Locate every Babesia divergens-infected red blood cell.
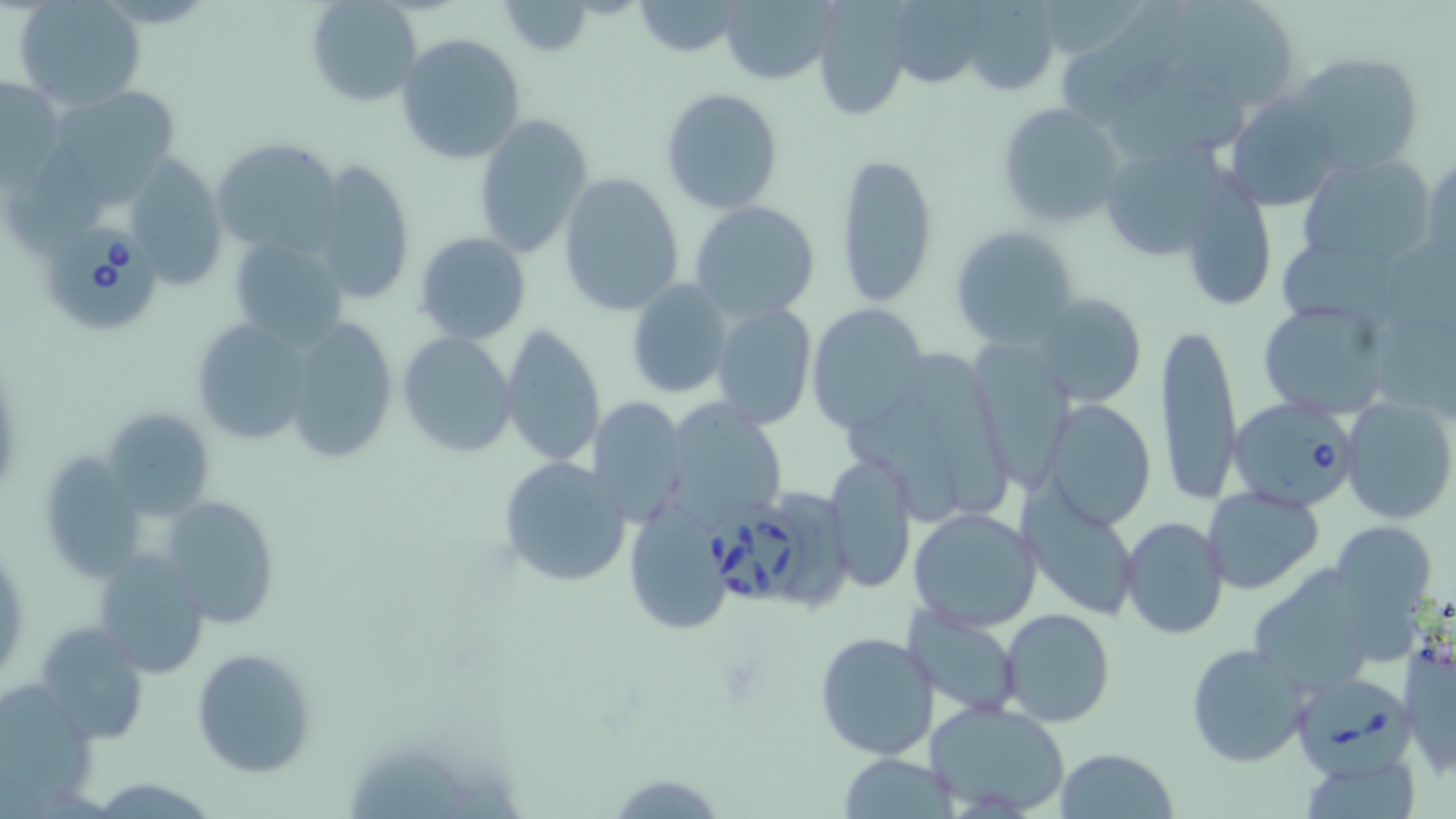

Approximate bounding boxes as (x1, y1, x2, y2) in pixels.
Babesia divergens-infected red blood cells: (45, 223, 158, 331), (1232, 397, 1360, 514), (706, 503, 811, 608), (1288, 673, 1414, 776).

Summary:
  - Uninfected red blood cell locations: (305, 0, 422, 107), (964, 0, 1058, 92), (1182, 0, 1300, 102), (13, 1, 147, 112), (499, 1, 595, 57), (633, 1, 744, 56), (720, 1, 838, 85), (1064, 4, 1190, 121), (813, 5, 908, 120), (395, 33, 525, 165), (1110, 50, 1250, 162), (1293, 51, 1424, 175), (1, 74, 68, 186), (49, 82, 183, 195), (660, 88, 782, 213), (1224, 92, 1341, 209), (994, 101, 1127, 228), (474, 112, 594, 259), (212, 138, 343, 262), (1110, 145, 1233, 261), (837, 152, 938, 307), (1422, 153, 1455, 272), (1296, 154, 1434, 267), (16, 155, 109, 248), (133, 155, 229, 290), (303, 158, 417, 308), (558, 171, 687, 317), (1179, 174, 1276, 312), (688, 201, 821, 323), (950, 226, 1081, 349), (414, 232, 531, 344), (223, 233, 347, 348), (1283, 243, 1402, 325), (626, 278, 732, 398), (1028, 291, 1148, 408), (1255, 295, 1395, 417), (711, 301, 816, 430), (806, 304, 928, 434), (188, 314, 318, 447), (282, 317, 400, 464), (1156, 318, 1241, 507), (500, 324, 605, 470), (397, 332, 519, 458), (971, 342, 1080, 491), (916, 359, 1012, 515), (843, 387, 976, 523), (1042, 397, 1156, 529), (585, 398, 689, 524), (1341, 398, 1456, 525), (663, 400, 789, 528), (101, 408, 215, 520), (38, 450, 150, 584), (823, 453, 917, 595), (497, 455, 632, 588), (1202, 486, 1325, 594), (784, 488, 857, 614), (1019, 489, 1141, 622), (160, 496, 280, 627), (622, 504, 736, 636), (908, 505, 1042, 632), (1119, 516, 1228, 640), (1330, 522, 1441, 635), (93, 549, 213, 677), (1254, 563, 1368, 689), (903, 605, 1025, 718), (1001, 608, 1114, 728), (32, 621, 151, 742), (813, 631, 941, 762), (1401, 635, 1455, 775), (1185, 642, 1312, 766), (190, 648, 315, 776), (4, 676, 92, 787), (928, 699, 1072, 815), (1055, 747, 1178, 819), (838, 755, 962, 816), (1307, 762, 1421, 819)
  - Slide-level diagnosis: Babesia divergens
  - Stain: May-Grünwald-Giemsa
  - Modality: light microscopy
  - Magnification: 1000x
  - Preparation: thin blood smear
  - Field of view: single
  - Image size: 1456×819 pixels